Outline each Plasmodium ovale-infected red blood cell.
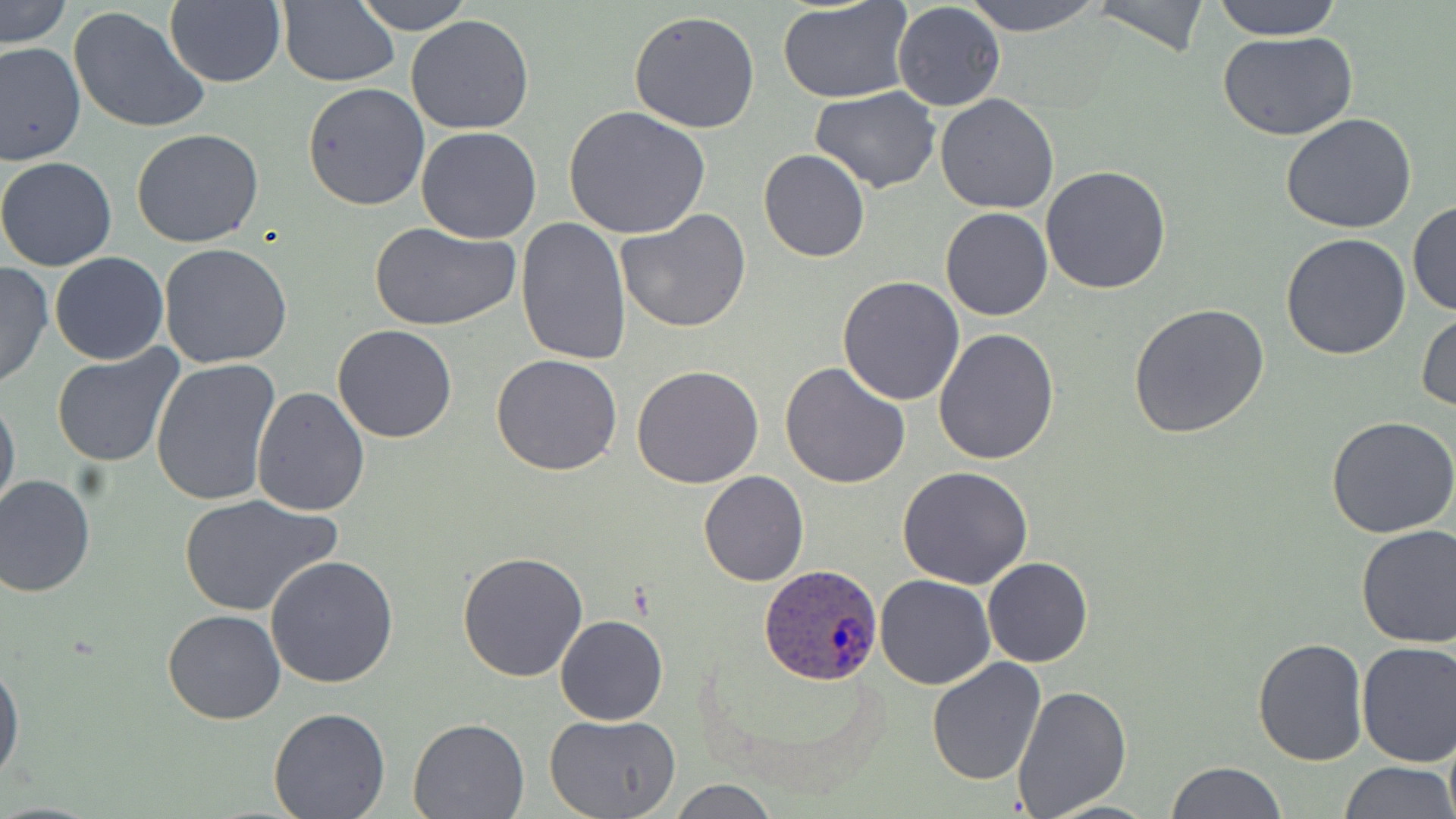
Approximate bounding boxes as [x1, y1, x2, y2] in pixels.
Plasmodium ovale-infected red blood cells: [760, 563, 883, 684].

slide_level_diagnosis: Plasmodium ovale
modality: light microscopy
preparation: thin blood film
field_of_view: single
stain: May-Grünwald-Giemsa
uninfected_red_blood_cell_locations: 'approximate bounding boxes as [x1, y1, x2, y2] in pixels: [2, 0, 71, 50], [351, 0, 472, 35], [964, 0, 1101, 36], [1089, 0, 1211, 60], [1210, 0, 1345, 40], [164, 1, 285, 87], [278, 1, 400, 86], [777, 2, 915, 104], [893, 3, 1005, 112], [67, 5, 213, 135], [629, 10, 761, 134], [405, 15, 534, 135], [1218, 30, 1358, 141], [1, 41, 85, 167], [302, 82, 431, 212], [811, 87, 942, 194], [934, 94, 1059, 214], [563, 106, 712, 239], [1279, 112, 1417, 234], [131, 128, 264, 248], [416, 128, 543, 244], [758, 149, 870, 262], [0, 156, 118, 271], [1040, 166, 1172, 295], [1407, 198, 1456, 316], [940, 206, 1052, 321], [617, 209, 752, 333], [516, 217, 631, 366], [367, 219, 520, 332], [1279, 233, 1411, 360], [159, 244, 293, 369], [49, 253, 169, 365], [0, 263, 52, 392], [838, 276, 965, 406], [1128, 302, 1270, 439], [1416, 309, 1456, 416], [333, 325, 456, 443], [934, 328, 1059, 465], [51, 346, 185, 467], [491, 354, 623, 476], [150, 358, 281, 508], [781, 362, 910, 487], [632, 365, 764, 487], [251, 385, 372, 517], [0, 393, 20, 519], [1327, 415, 1456, 538], [898, 465, 1033, 588], [699, 470, 808, 586], [0, 472, 96, 597], [178, 493, 341, 617], [1355, 523, 1456, 647], [457, 551, 588, 683], [265, 555, 400, 689], [983, 556, 1093, 668], [876, 575, 995, 690], [163, 610, 286, 725], [556, 615, 668, 726], [1253, 637, 1368, 766], [1356, 641, 1456, 768], [0, 659, 23, 783], [927, 659, 1046, 786], [1012, 685, 1132, 817], [268, 708, 391, 819], [544, 714, 680, 819], [408, 716, 531, 818], [1166, 761, 1286, 818], [1340, 761, 1453, 818], [668, 780, 778, 818]'
magnification: 1000x
image_size: 1456×819 pixels